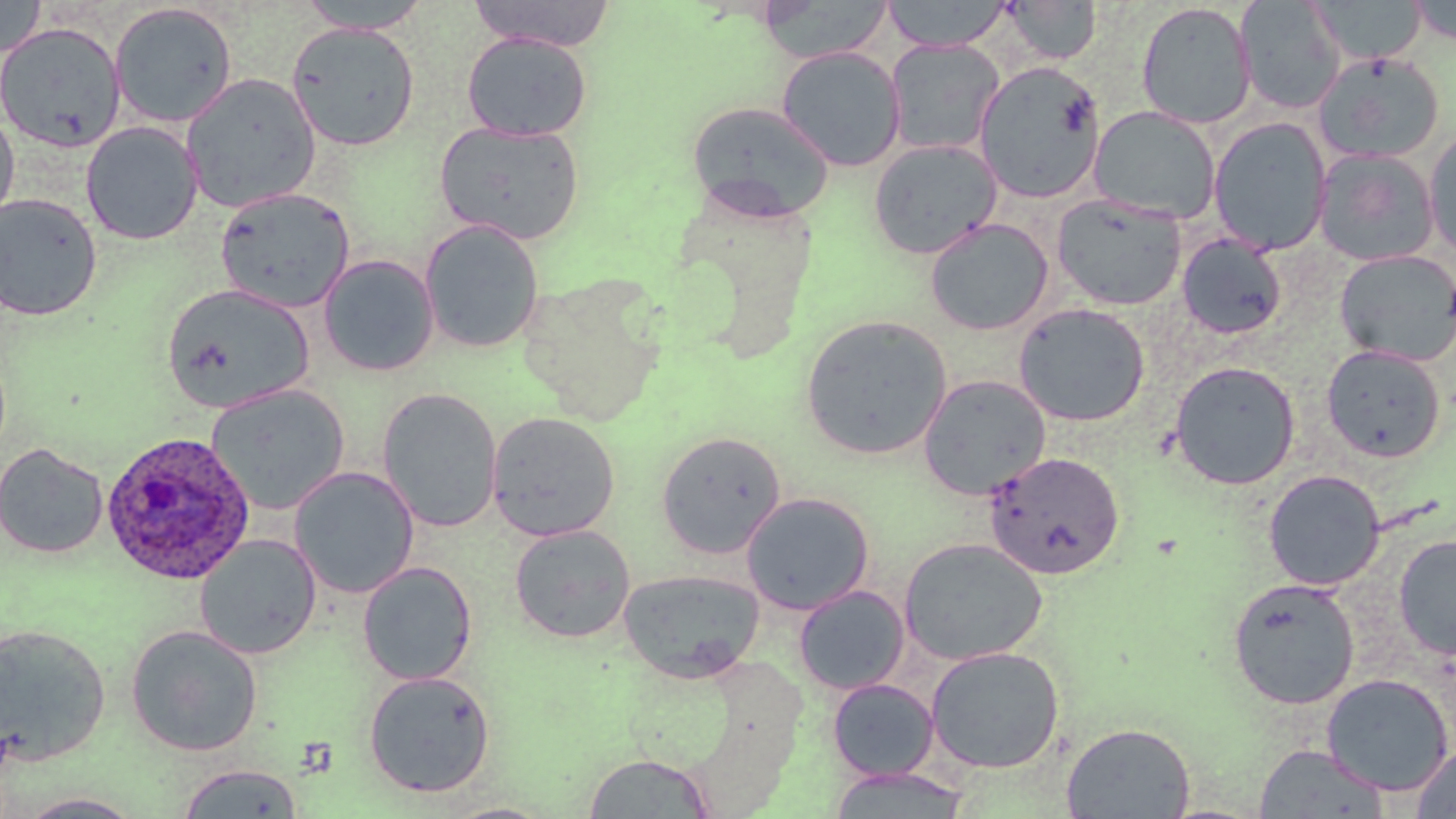

Summary:
  - Coordinate format: approximate bounding boxes as (x1,y1)-(x2,y2) corner pairs in pixels
  - Plasmodium ovale-infected red blood cell locations: (98,430)-(256,585)
  - Uninfected red blood cell locations: (0,0)-(46,58), (295,0)-(433,33), (467,0)-(617,51), (882,0)-(1011,52), (1308,0)-(1426,67), (755,1)-(894,63), (1001,1)-(1102,66), (1235,1)-(1346,114), (1136,2)-(1256,129), (1409,2)-(1456,45), (109,3)-(238,128), (286,21)-(421,151), (0,22)-(126,153), (462,32)-(591,141), (886,39)-(1004,155), (776,46)-(906,171), (1313,52)-(1445,164), (973,60)-(1107,203), (182,73)-(321,213), (686,100)-(835,221), (1089,106)-(1221,223), (0,107)-(20,229), (1208,116)-(1332,255), (434,120)-(586,245), (81,121)-(203,245), (1424,126)-(1456,261), (868,138)-(1002,260), (1314,149)-(1440,267), (216,187)-(355,312), (0,193)-(103,321), (1051,193)-(1187,310), (924,217)-(1054,336), (420,219)-(544,354), (1177,234)-(1287,339), (1334,250)-(1456,366), (319,254)-(439,376), (161,283)-(314,413), (1013,302)-(1150,427), (801,314)-(952,460), (1321,344)-(1446,462), (1169,361)-(1300,490), (918,374)-(1052,500), (207,384)-(349,514), (376,388)-(503,532), (486,411)-(620,542), (655,430)-(786,558), (0,443)-(109,560), (983,451)-(1125,580), (289,466)-(419,599), (1263,469)-(1385,590), (740,492)-(875,615), (509,524)-(636,644), (194,534)-(322,659), (1394,534)-(1456,660), (899,537)-(1047,665), (357,561)-(477,686), (618,569)-(765,684), (1227,577)-(1361,710), (794,585)-(910,694), (0,623)-(112,764), (125,624)-(263,756), (925,646)-(1065,774), (363,670)-(496,798), (1321,674)-(1453,796), (827,678)-(940,781), (1060,722)-(1196,818), (1253,743)-(1389,818), (1410,744)-(1456,818), (583,752)-(716,817), (176,763)-(305,818), (826,766)-(973,817), (17,793)-(146,818)
  - Slide-level diagnosis: Plasmodium ovale
  - Image size: 1456×819 pixels
  - Field of view: single
  - Preparation: thin blood film
  - Stain: May-Grünwald-Giemsa
  - Magnification: 1000x
  - Modality: light microscopy